Locate platelets.
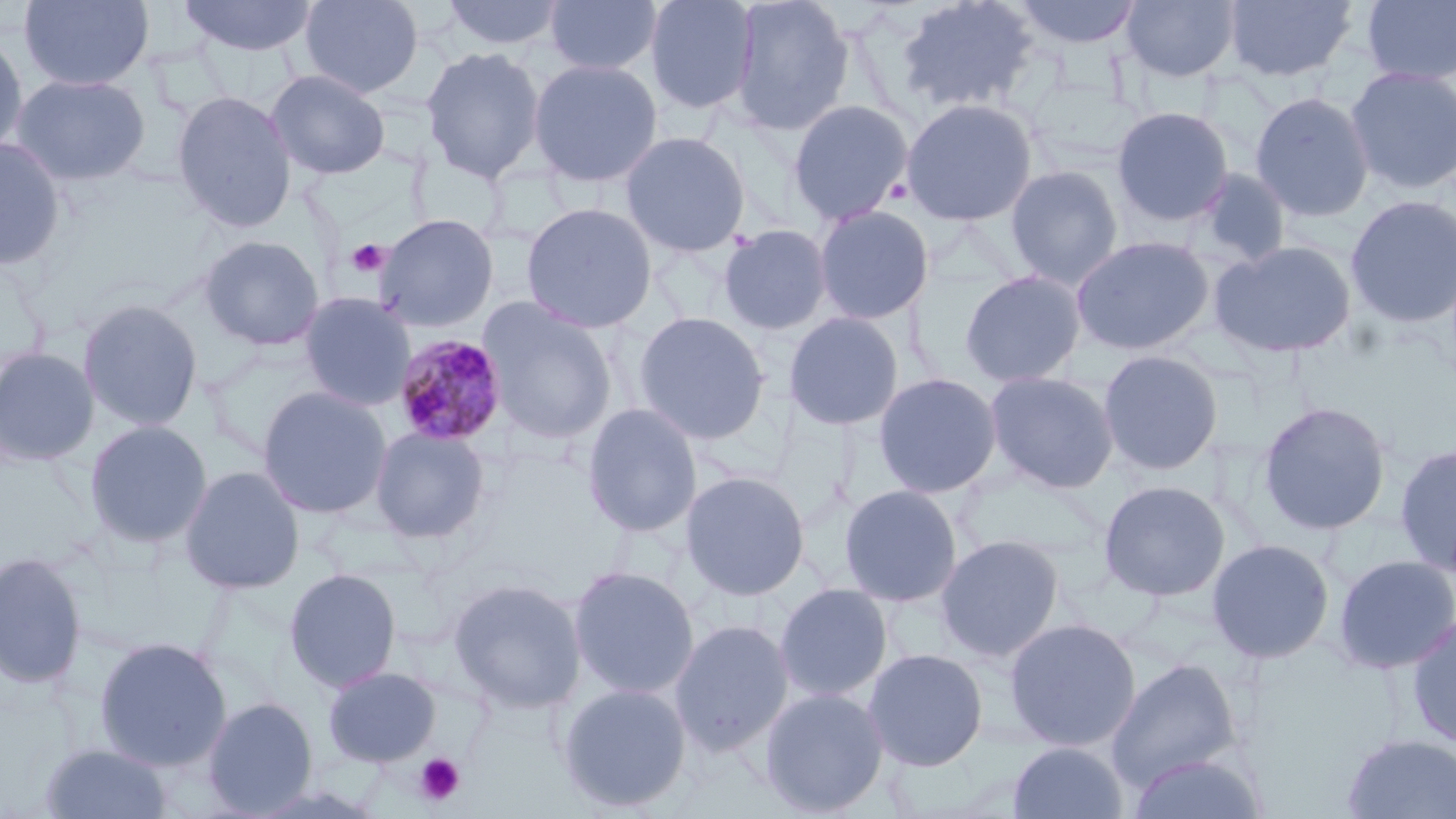

Approximate bounding boxes as [x1, y1, x2, y2] in pixels.
Platelets: [346, 239, 389, 278], [414, 752, 465, 806].

slide-level diagnosis = Plasmodium malariae
image size = 1456×819 pixels
magnification = 1000x
field of view = one of a larger specimen
modality = light microscopy
Plasmodium malariae-infected red blood cell locations = approximate bounding boxes as [x1, y1, x2, y2] in pixels: [393, 334, 508, 448]
stain = May-Grünwald-Giemsa
preparation = thin blood film
uninfected red blood cell locations = approximate bounding boxes as [x1, y1, x2, y2] in pixels: [19, 0, 154, 92], [178, 0, 318, 56], [299, 0, 423, 98], [440, 0, 565, 52], [544, 0, 662, 76], [644, 0, 760, 115], [727, 0, 855, 137], [895, 0, 1040, 114], [1013, 0, 1142, 49], [1121, 0, 1240, 82], [1223, 0, 1358, 83], [1361, 0, 1456, 86], [0, 29, 29, 159], [421, 46, 545, 184], [528, 58, 663, 187], [1345, 66, 1456, 196], [266, 69, 391, 180], [11, 73, 151, 186], [171, 90, 297, 233], [1250, 91, 1375, 222], [900, 97, 1039, 227], [787, 98, 914, 225], [1110, 106, 1234, 227], [619, 130, 751, 258], [0, 137, 67, 272], [1005, 165, 1124, 288], [1188, 167, 1294, 270], [1196, 179, 1319, 342], [1345, 194, 1456, 329], [520, 201, 658, 333], [813, 204, 935, 325], [375, 213, 499, 332], [718, 224, 834, 336], [198, 235, 325, 351], [1071, 235, 1214, 356], [1210, 240, 1358, 359], [959, 269, 1087, 388], [298, 292, 416, 411], [78, 298, 204, 433], [478, 298, 618, 445], [633, 311, 771, 445], [783, 311, 905, 432], [0, 346, 100, 467], [1098, 349, 1224, 475], [984, 370, 1119, 493], [872, 372, 1002, 499], [256, 386, 393, 519], [1257, 401, 1392, 536], [581, 403, 702, 537], [84, 420, 212, 549], [369, 425, 491, 543], [1394, 442, 1456, 578], [179, 465, 305, 595], [680, 470, 811, 601], [1098, 479, 1231, 602], [838, 484, 963, 607], [935, 534, 1066, 662], [1206, 538, 1335, 664], [0, 551, 87, 691], [1332, 554, 1456, 675], [568, 565, 700, 700], [283, 568, 402, 692], [447, 577, 587, 715], [774, 582, 893, 702], [1405, 613, 1456, 749], [1004, 617, 1141, 752], [669, 619, 794, 756], [93, 636, 232, 772], [864, 647, 988, 771], [1105, 657, 1243, 790], [323, 666, 441, 767], [556, 682, 692, 813], [759, 686, 889, 817], [203, 697, 318, 817], [1340, 733, 1456, 819], [1008, 740, 1129, 819], [39, 743, 175, 819], [1125, 749, 1269, 819]